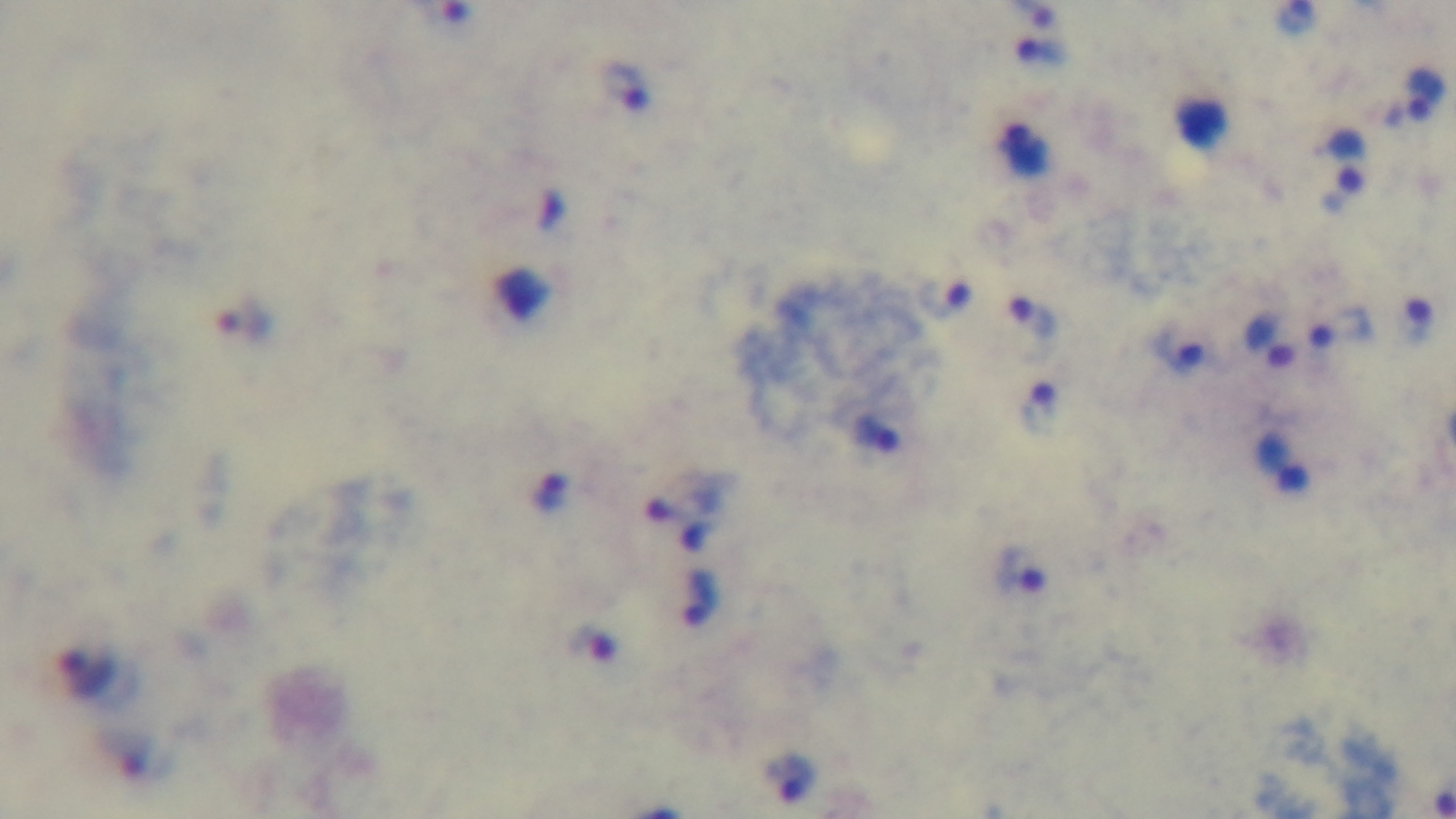

Giemsa-stained. Captured with a mounted 4K digital camera. 100x oil-immersion objective. Photomicrograph. Malaria status: positive. Single field of view. Preparation: thick smear.